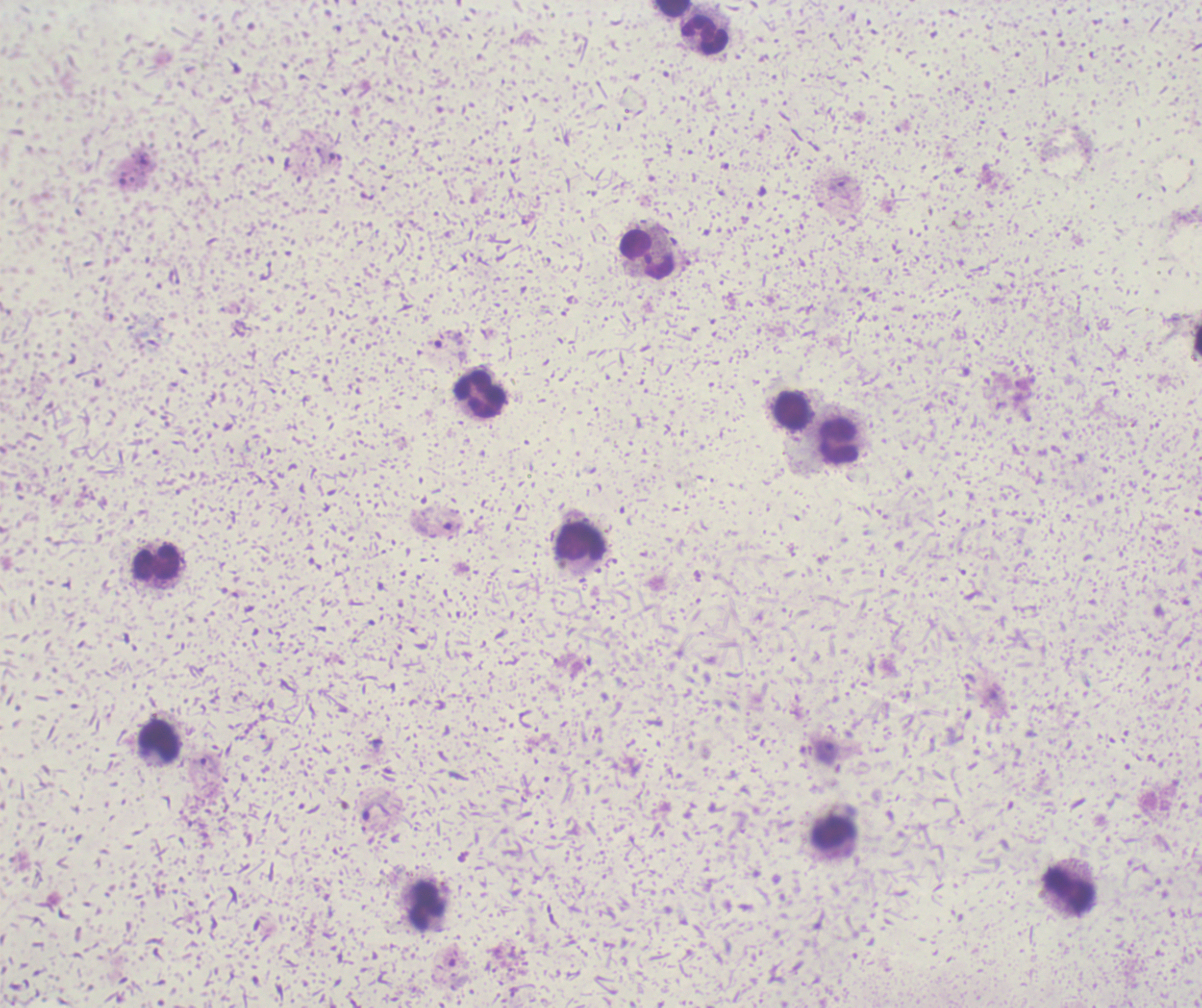

coordinate format = approximate object centers, in pixels from the top-left corner
trophozoite locations = (x=826, y=754), (x=209, y=764)
leukocyte locations = (x=672, y=8), (x=706, y=35), (x=646, y=255), (x=479, y=394), (x=792, y=411), (x=839, y=441), (x=579, y=542), (x=155, y=564), (x=159, y=740), (x=1069, y=891), (x=427, y=905)
image size = 1202×1008 pixels
result = Plasmodium parasites identified
preparation = thick blood smear
background quality = unsatisfactory
context = previously used in an actual diagnosis
magnification = 100x
stain = Romanowsky
field of view = one from this slide